Comment on the morphology of the erythrocytes.
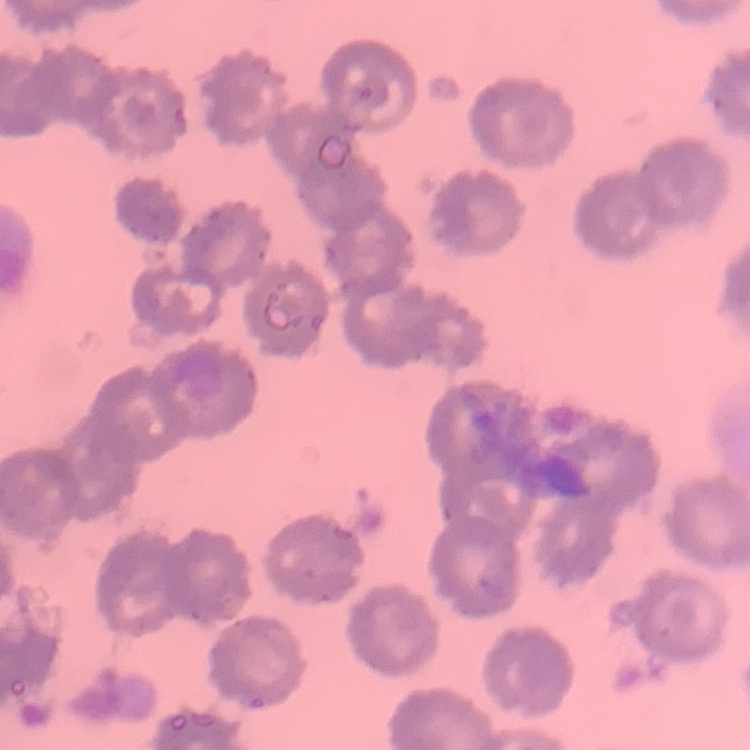

They show no rouleaux formation.

Summary:
  - Stain: Field's or Giemsa
  - Preparation: thin blood film
  - Image type: one tile cut from a larger photomicrograph